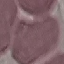

malaria status = uninfected
stain = Giemsa
capture = smartphone camera at the microscope eyepiece
preparation = thin blood film
image type = automatically extracted cell patch, resized to 64 × 64 pixels